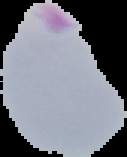
Result: Plasmodium parasites identified. Image is 127×157 pixels. Segmented cell region on a black background. From a thin blood film.